Report the malaria status.
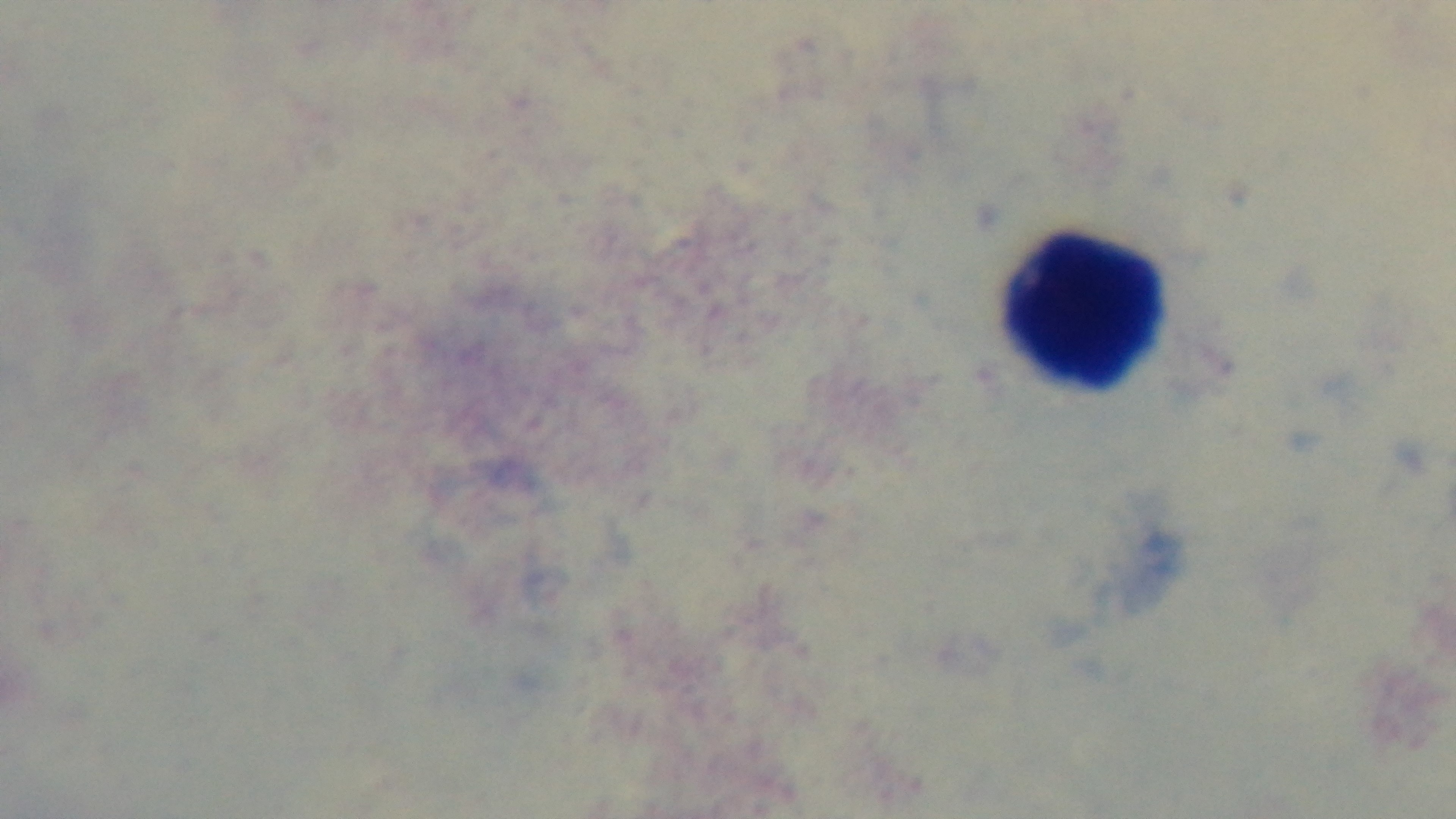

It is uninfected.

{
  "field_of_view": "single",
  "capture": "mounted 4K digital camera",
  "preparation": "thick smear",
  "stain": "Giemsa",
  "objective": "100x oil immersion",
  "modality": "light microscopy"
}